State which parasite is depicted.
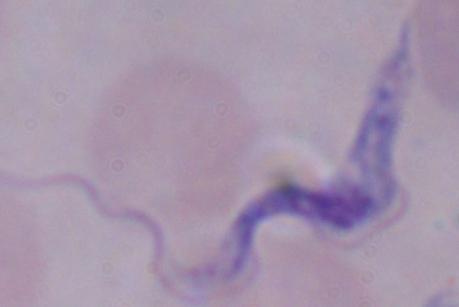

A trypanosome.

Summary:
  - Modality: photomicrograph
  - Magnification: 1000x